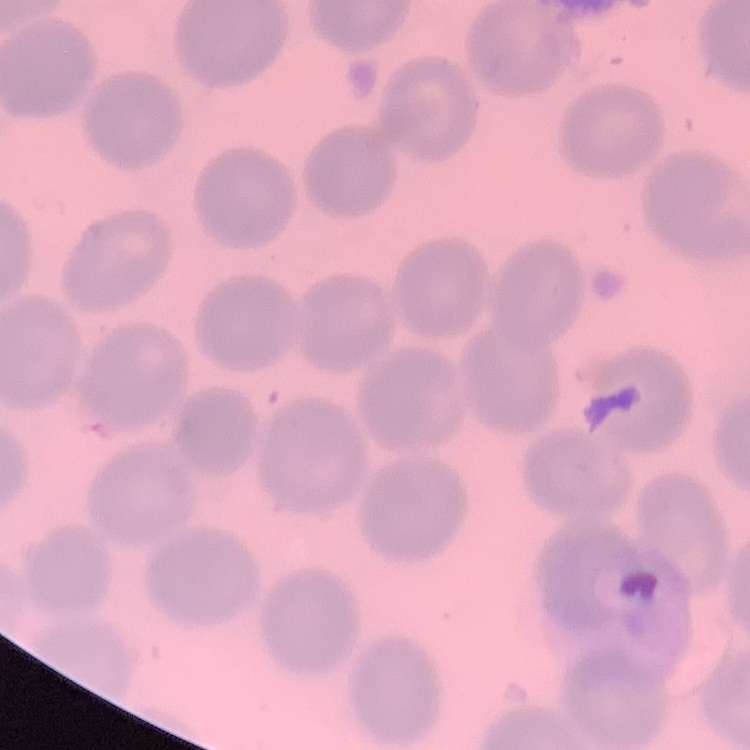
red blood cell morphology = no rouleaux formation
preparation = thin blood smear
image type = one tile cut from a larger photomicrograph
stain = Field's or Giemsa